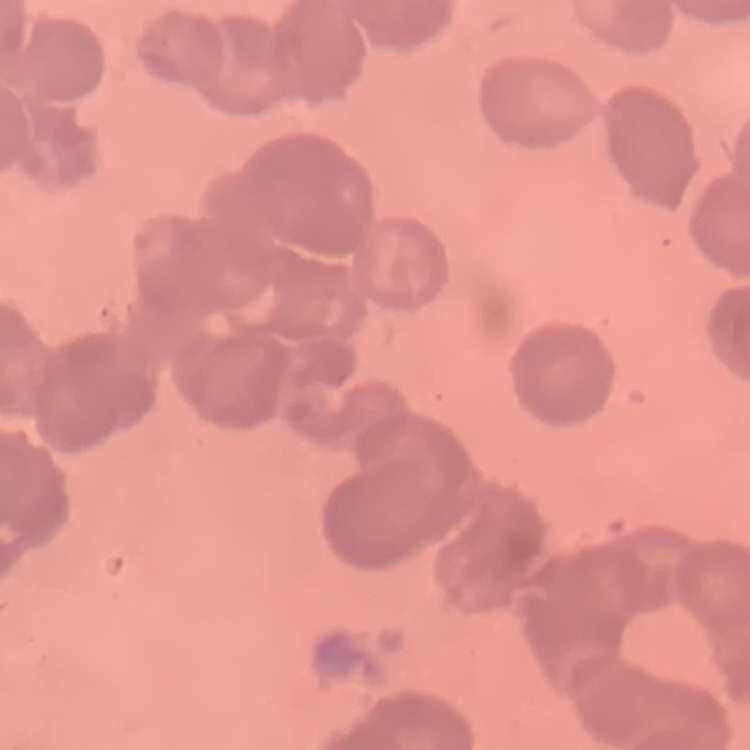 The red blood cells show rouleaux formation. Square crop of a larger photomicrograph. Thin blood smear. Field's or Giemsa stain.